Report the malaria status of this cell.
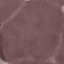
Uninfected.

Cell patch, automatically extracted from a larger field of view and resized to 64 × 64 pixels. Thin blood film. Photographed with a smartphone camera at the microscope eyepiece. Giemsa-stained preparation.